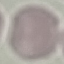
Summary:
  - Result: no malaria parasites detected
  - Stain: Giemsa
  - Image type: automatically extracted cell patch, resized to 64 × 64 pixels
  - Capture: smartphone camera at the microscope eyepiece
  - Preparation: thin blood film